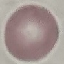
Malaria status: uninfected. Acquired by smartphone through the microscope eyepiece. Giemsa-stained preparation. Thin blood film. Cell patch, automatically extracted from a larger field of view and resized to 64 × 64 pixels.